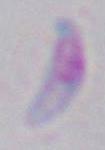

identification = Toxoplasma gondii
modality = micrograph
magnification = 1000x